Classify this cell by malaria status.
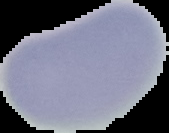
It is uninfected.

Summary:
  - Image size: 169×133 pixels
  - Preparation: thin blood smear
  - Image type: segmented cell region with the area outside set to black